Locate every blood parasite and identify its species.
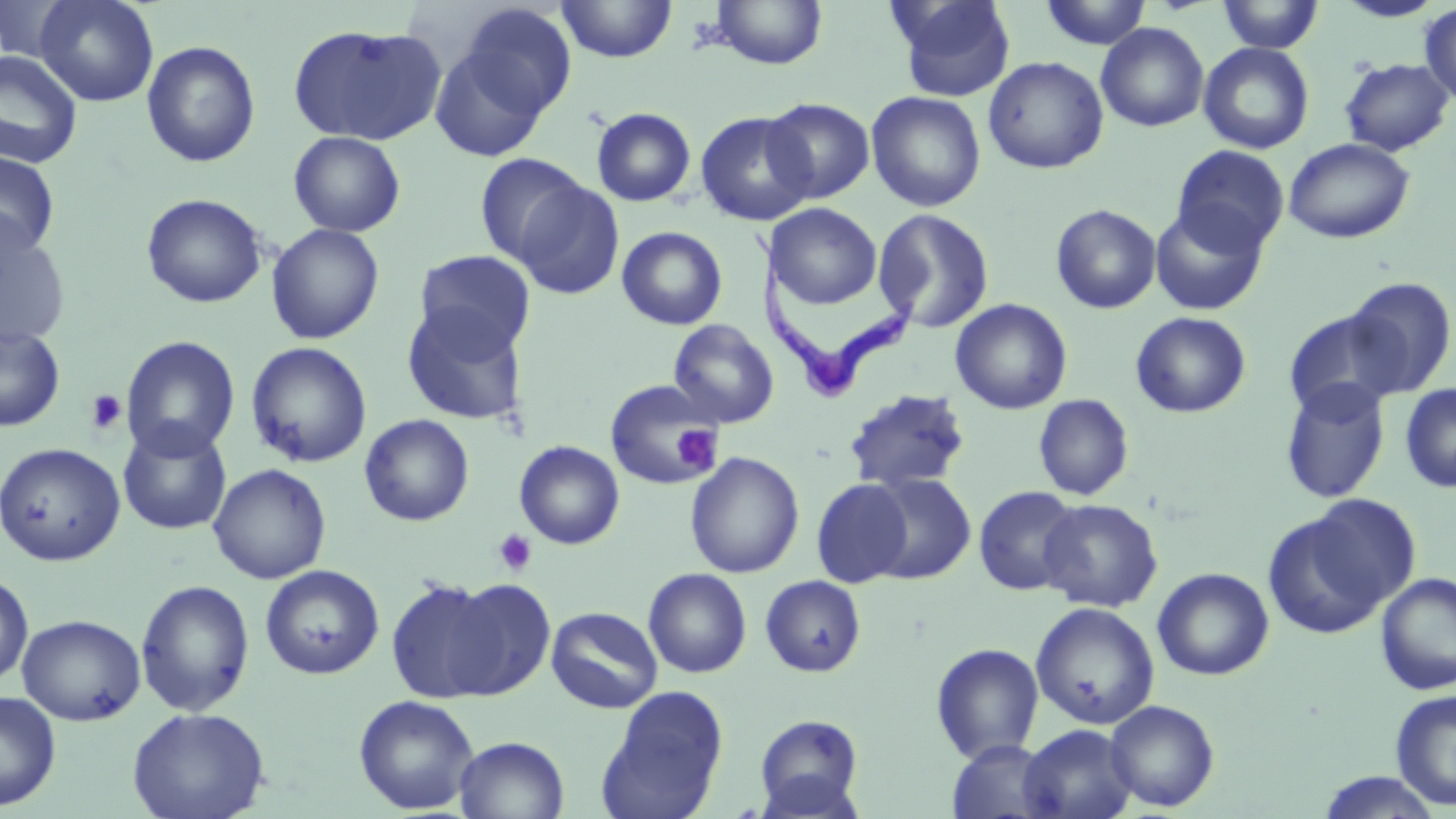

Approximate bounding boxes as named x1/y1/x2/y2 corners in pixels.
Trypanosoma brucei: (x1=753, y1=230, x2=920, y2=405).
No Plasmodium falciparum, Plasmodium ovale, Plasmodium malariae, Plasmodium vivax, or Babesia divergens observed.

slide_level_diagnosis: Trypanosoma brucei
preparation: thin blood smear
field_of_view: single
magnification: 1000x
modality: optical microscopy
image_size: 1456×819 pixels
uninfected_red_blood_cell_locations: 'approximate bounding boxes as named x1/y1/x2/y2 corners in pixels: (x1=0, y1=0, x2=78, y2=63), (x1=34, y1=0, x2=158, y2=106), (x1=890, y1=0, x2=1017, y2=102), (x1=1039, y1=0, x2=1153, y2=50), (x1=1333, y1=0, x2=1447, y2=22), (x1=556, y1=1, x2=677, y2=63), (x1=710, y1=1, x2=828, y2=70), (x1=1216, y1=1, x2=1324, y2=53), (x1=456, y1=3, x2=577, y2=121), (x1=1419, y1=3, x2=1456, y2=106), (x1=1096, y1=22, x2=1209, y2=132), (x1=288, y1=23, x2=447, y2=145), (x1=141, y1=40, x2=261, y2=168), (x1=429, y1=41, x2=554, y2=162), (x1=1199, y1=41, x2=1314, y2=154), (x1=0, y1=50, x2=83, y2=169), (x1=983, y1=56, x2=1108, y2=174), (x1=1339, y1=57, x2=1454, y2=157), (x1=866, y1=91, x2=985, y2=211), (x1=762, y1=98, x2=875, y2=204), (x1=590, y1=107, x2=697, y2=207), (x1=695, y1=110, x2=816, y2=226), (x1=288, y1=130, x2=406, y2=237), (x1=1283, y1=137, x2=1415, y2=244), (x1=1172, y1=145, x2=1290, y2=254), (x1=0, y1=150, x2=60, y2=258), (x1=474, y1=153, x2=589, y2=266), (x1=512, y1=180, x2=625, y2=300), (x1=141, y1=193, x2=267, y2=308), (x1=766, y1=203, x2=882, y2=309), (x1=1050, y1=204, x2=1161, y2=314), (x1=1150, y1=204, x2=1269, y2=315), (x1=873, y1=208, x2=994, y2=333), (x1=0, y1=215, x2=71, y2=348), (x1=266, y1=223, x2=385, y2=345), (x1=617, y1=226, x2=728, y2=330), (x1=414, y1=250, x2=536, y2=357), (x1=1343, y1=277, x2=1455, y2=398), (x1=951, y1=299, x2=1072, y2=414), (x1=401, y1=304, x2=528, y2=425), (x1=1283, y1=309, x2=1406, y2=419), (x1=1130, y1=311, x2=1251, y2=418), (x1=668, y1=319, x2=779, y2=428), (x1=0, y1=322, x2=65, y2=432), (x1=119, y1=335, x2=241, y2=460), (x1=245, y1=341, x2=372, y2=468), (x1=604, y1=378, x2=723, y2=489), (x1=1280, y1=379, x2=1390, y2=503), (x1=1399, y1=382, x2=1456, y2=493), (x1=843, y1=389, x2=972, y2=495), (x1=1033, y1=393, x2=1134, y2=501), (x1=359, y1=414, x2=474, y2=526), (x1=117, y1=422, x2=232, y2=535), (x1=514, y1=440, x2=624, y2=550), (x1=0, y1=442, x2=125, y2=566), (x1=684, y1=451, x2=804, y2=578), (x1=208, y1=463, x2=331, y2=585), (x1=864, y1=473, x2=975, y2=584), (x1=811, y1=478, x2=915, y2=588), (x1=973, y1=486, x2=1083, y2=596), (x1=1039, y1=498, x2=1162, y2=612), (x1=1263, y1=505, x2=1398, y2=638), (x1=260, y1=565, x2=384, y2=680), (x1=1152, y1=567, x2=1274, y2=680), (x1=643, y1=568, x2=752, y2=678), (x1=1374, y1=572, x2=1456, y2=695), (x1=0, y1=573, x2=34, y2=687), (x1=760, y1=575, x2=866, y2=677), (x1=439, y1=576, x2=556, y2=700), (x1=135, y1=578, x2=255, y2=717), (x1=385, y1=578, x2=506, y2=703), (x1=1030, y1=602, x2=1160, y2=730), (x1=546, y1=606, x2=662, y2=713), (x1=17, y1=614, x2=146, y2=726), (x1=930, y1=643, x2=1045, y2=764), (x1=598, y1=686, x2=728, y2=819), (x1=1391, y1=689, x2=1456, y2=811), (x1=0, y1=690, x2=61, y2=811), (x1=353, y1=694, x2=479, y2=814), (x1=1104, y1=699, x2=1220, y2=812), (x1=126, y1=706, x2=270, y2=819), (x1=754, y1=713, x2=865, y2=815), (x1=1019, y1=724, x2=1138, y2=819), (x1=454, y1=735, x2=570, y2=819), (x1=947, y1=740, x2=1058, y2=819), (x1=1314, y1=772, x2=1444, y2=818)'
stain: May-Grünwald-Giemsa
platelet_locations: 'approximate bounding boxes as named x1/y1/x2/y2 corners in pixels: (x1=85, y1=389, x2=127, y2=435), (x1=671, y1=425, x2=720, y2=473), (x1=493, y1=528, x2=536, y2=576)'